Describe the morphology of the red blood cells.
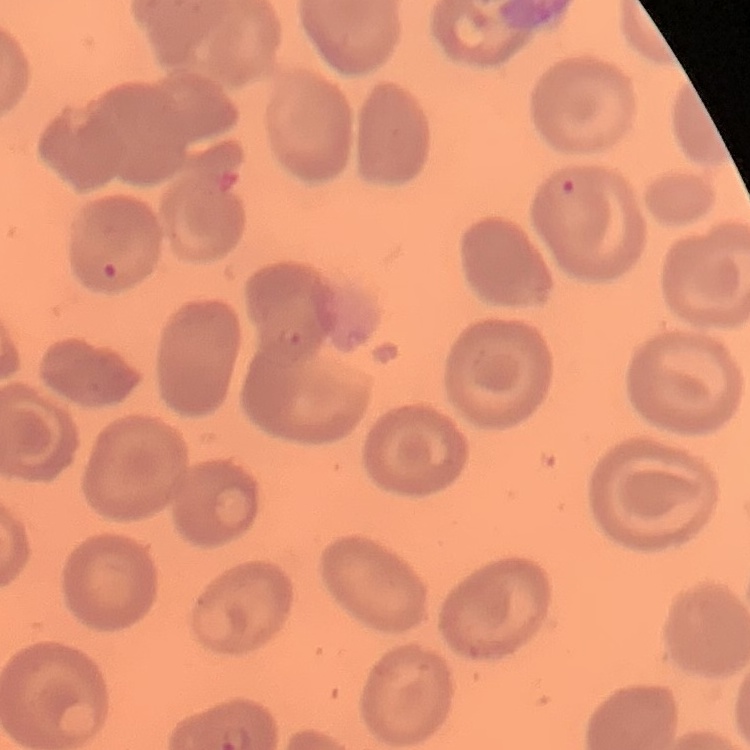

They show no rouleaux formation.

Thin blood film. Field's or Giemsa stain. One tile cut from a larger photomicrograph.